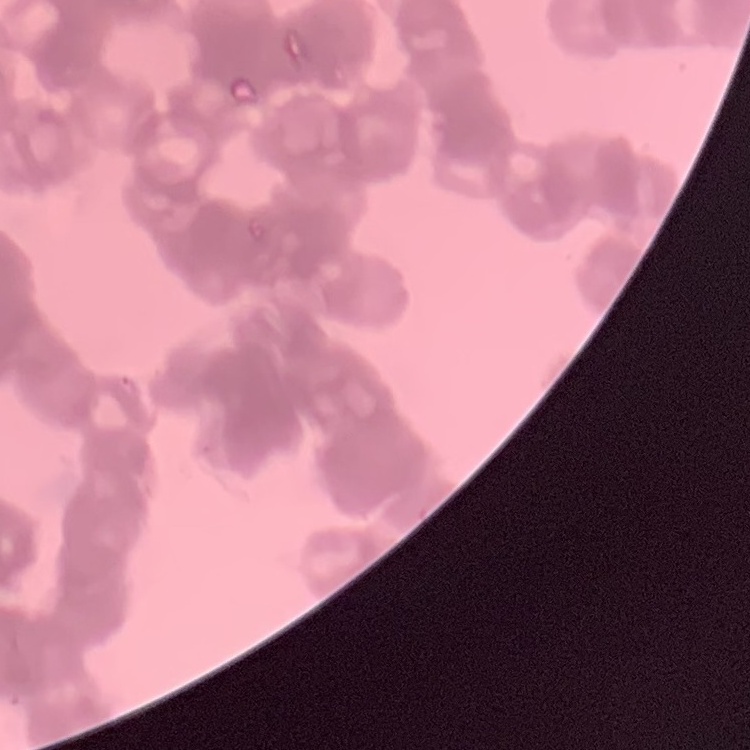 The erythrocytes exhibit rouleaux formation. Field's or Giemsa stain. One tile cut from a larger photomicrograph. Thin blood film.